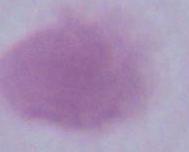

Summary:
  - Modality: photomicrograph
  - Identification: red blood cell
  - Magnification: 1000x